Locate every leukocyte (white blood cell).
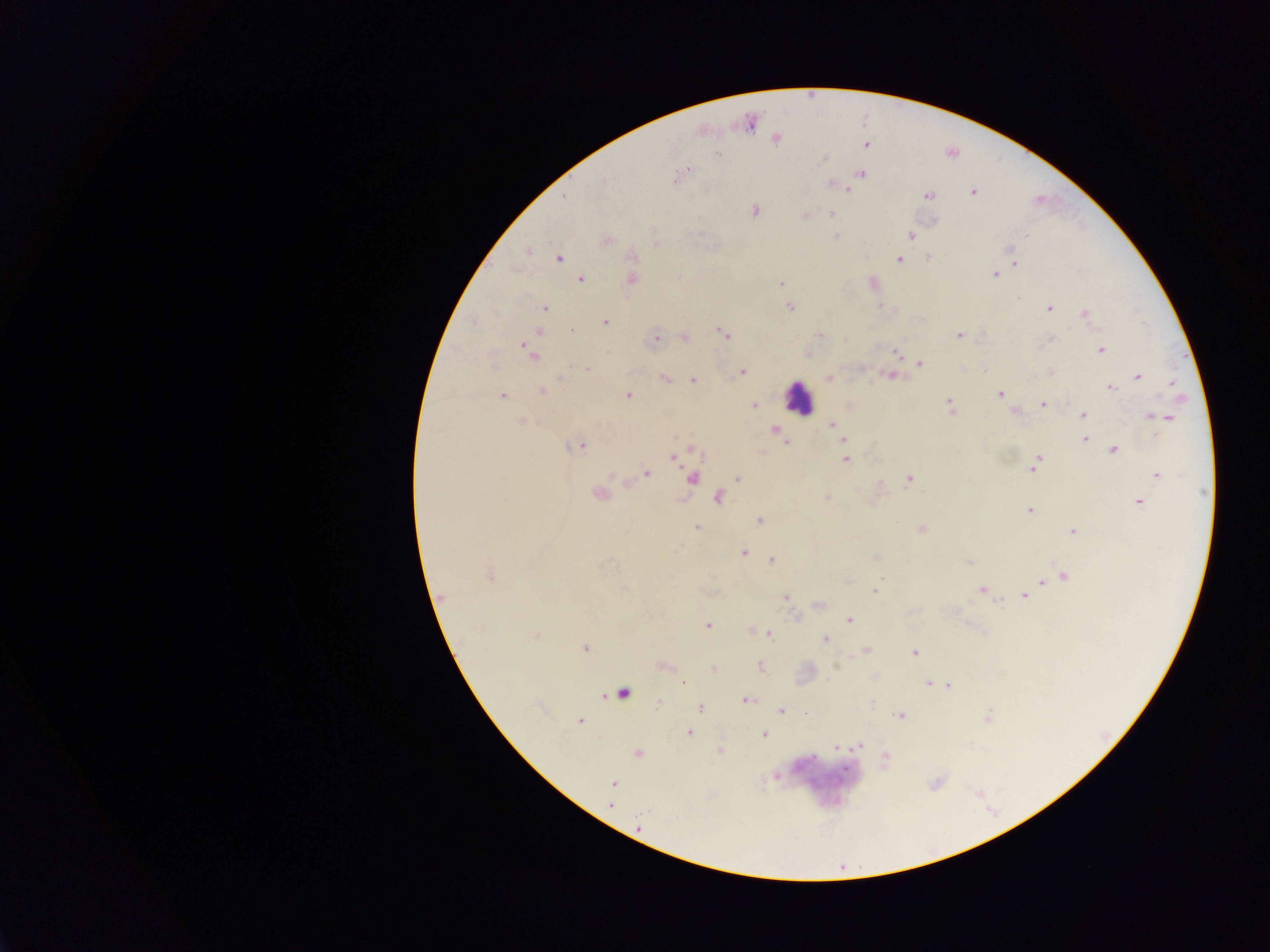
Approximate centers as (x, y) in pixels.
Leukocytes: (798, 397), (622, 693).

Summary:
  - Malaria parasite locations: (748, 122), (776, 139), (867, 145), (717, 154), (861, 173), (677, 177), (604, 181), (830, 184), (848, 188), (973, 192), (928, 195), (564, 196), (755, 210), (831, 213), (805, 216), (934, 221), (653, 231), (911, 235), (836, 236), (606, 240), (1011, 249), (528, 251), (929, 257), (559, 259), (898, 259), (1014, 262), (994, 274), (581, 279), (632, 279), (781, 283), (879, 306), (790, 307), (544, 308), (1048, 308), (1086, 314), (473, 322), (605, 322), (572, 331), (539, 333), (723, 333), (820, 334), (959, 335), (685, 337), (844, 338), (1051, 338), (656, 339), (1100, 350), (527, 352), (896, 352), (919, 363), (587, 369), (742, 372), (1050, 372), (890, 376), (1138, 376), (665, 379), (829, 379), (693, 380), (1171, 383), (1110, 387), (542, 390), (1000, 394), (502, 396), (628, 396), (1042, 404), (754, 406), (949, 406), (1014, 411), (1083, 415), (1152, 416), (1166, 418), (521, 421), (832, 425), (775, 430), (836, 431), (1085, 439), (787, 440), (844, 440), (579, 445), (1114, 450), (673, 457), (845, 459), (1036, 463), (646, 473), (1157, 475), (613, 477), (692, 478), (737, 478), (909, 479), (599, 494), (718, 497), (827, 498), (1139, 501), (1030, 510), (759, 521), (697, 528), (922, 529), (1074, 531), (743, 552), (875, 556), (773, 560), (969, 562), (489, 575), (1064, 576), (1043, 581), (982, 590), (874, 591), (786, 596), (1024, 596), (443, 597), (820, 604), (850, 620), (707, 625), (768, 634), (536, 635), (825, 640), (585, 648), (867, 650), (914, 652), (663, 666), (760, 667), (713, 669), (928, 683), (683, 684), (948, 686), (746, 700), (659, 703), (700, 707), (781, 711), (901, 716), (580, 721), (689, 733), (764, 735), (860, 745), (837, 748), (719, 751), (637, 754), (885, 755), (614, 783), (611, 805), (646, 812), (676, 817), (638, 826)
  - Field of view: single
  - Image size: 1270×952 pixels
  - Preparation: thick blood film
  - Capture: mobile-phone photograph through a microscope
  - Country: Ghana